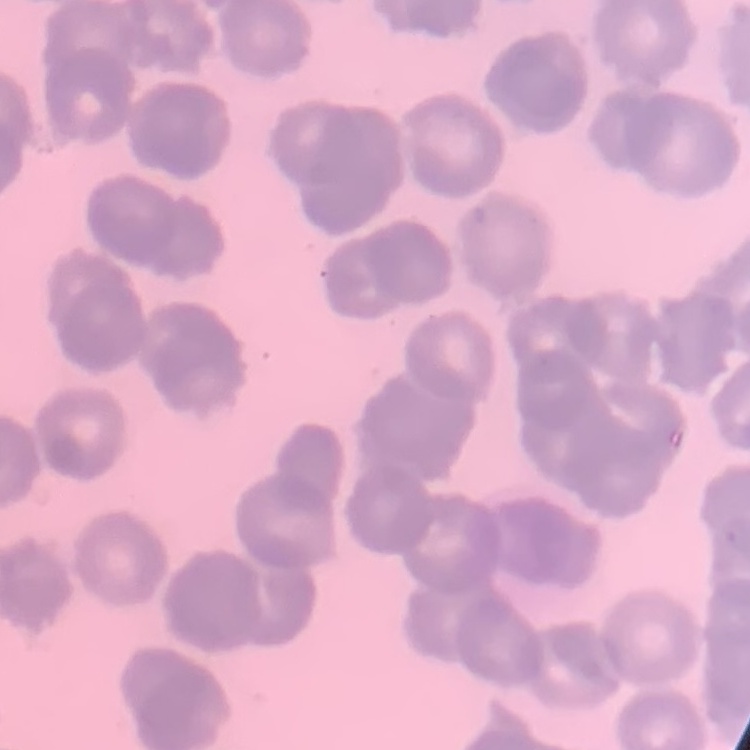

Summary:
  - Erythrocyte morphology: rouleaux formation
  - Image type: square crop of a larger photomicrograph
  - Preparation: thin peripheral smear
  - Stain: Field's or Giemsa